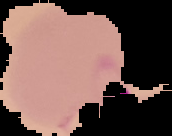

Summary:
  - Preparation: thin blood smear
  - Image size: 172×136 pixels
  - Image type: cell region segmented out of the field of view; surrounding area masked to black
  - Malaria status: parasitized